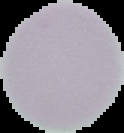

preparation = thin blood smear
image type = segmented cell region on a black background
image size = 124×133 pixels
result = negative for malaria parasites